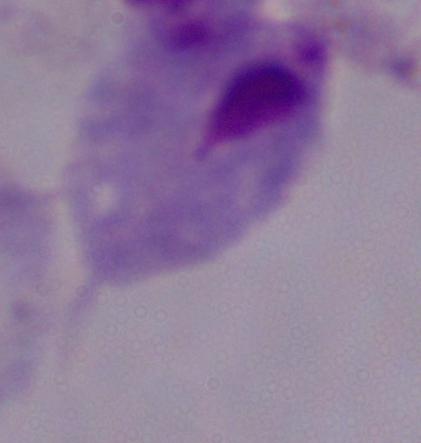

Summary:
  - Modality: photomicrograph
  - Magnification: 1000x
  - Identification: trichomonad